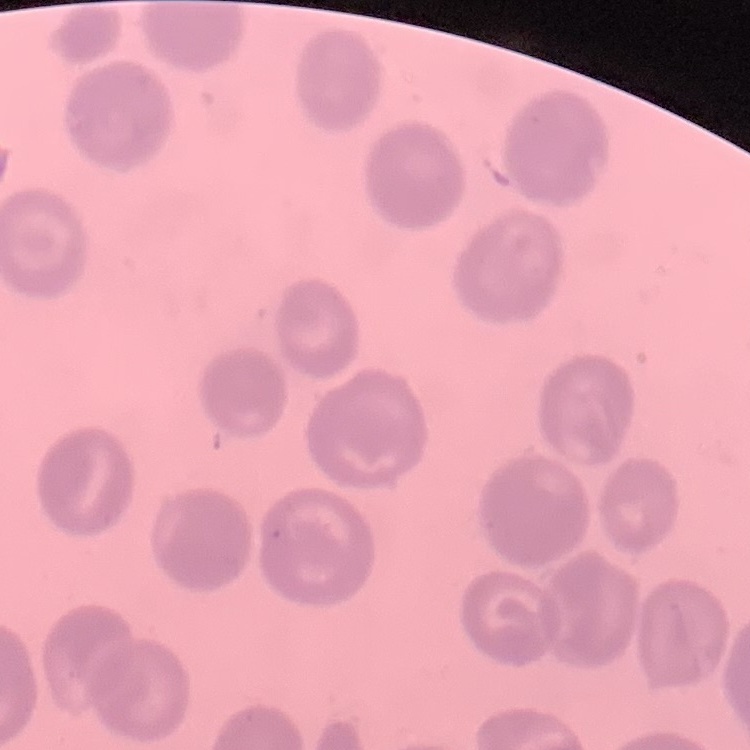
Summary:
  - Red blood cell morphology: no rouleaux formation
  - Preparation: thin blood smear
  - Stain: Field's or Giemsa
  - Image type: square crop of a larger photomicrograph